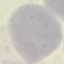

Summary:
  - Malaria status: uninfected
  - Stain: Giemsa
  - Preparation: thin blood film
  - Image type: automatically extracted cell patch, resized to 64 × 64 pixels
  - Capture: smartphone through the microscope eyepiece